Locate every Plasmodium parasite.
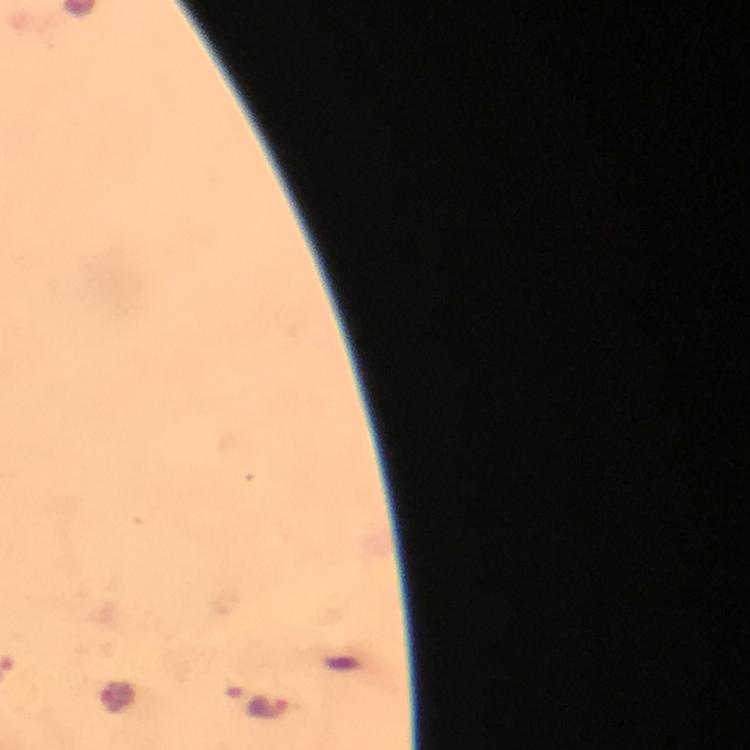

Approximate centers as [x, y] in pixels.
Plasmodium parasites: [271, 707].

{
  "preparation": "thick blood smear",
  "cropped_from": "a single field of view",
  "magnification": "100x",
  "capture": "smartphone camera through the microscope",
  "stain": "Giemsa",
  "image_size": "750×750 pixels",
  "context": "from a malaria diagnostic workup",
  "immersion_oil": "used"
}